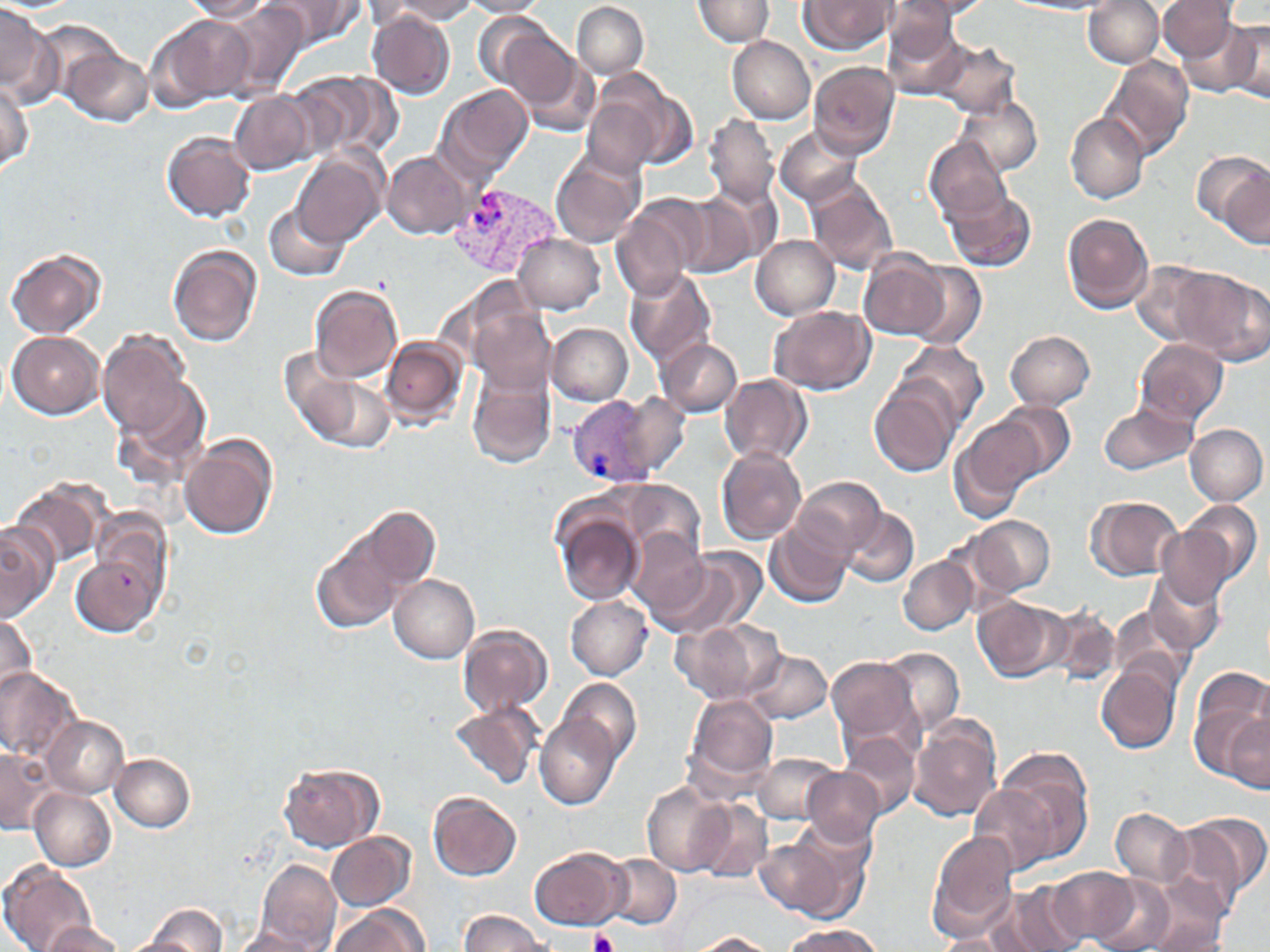

Summary:
  - Coordinate format: approximate bounding boxes as named x1/y1/x2/y2 corners in pixels
  - Uninfected red blood cell locations: (x1=180, y1=0, x2=274, y2=23), (x1=264, y1=0, x2=360, y2=47), (x1=380, y1=0, x2=479, y2=23), (x1=692, y1=0, x2=775, y2=45), (x1=798, y1=0, x2=894, y2=55), (x1=892, y1=0, x2=997, y2=22), (x1=462, y1=1, x2=550, y2=17), (x1=1083, y1=1, x2=1163, y2=67), (x1=1158, y1=1, x2=1242, y2=63), (x1=219, y1=2, x2=312, y2=97), (x1=363, y1=2, x2=455, y2=33), (x1=571, y1=2, x2=648, y2=79), (x1=885, y1=2, x2=984, y2=49), (x1=0, y1=3, x2=56, y2=100), (x1=366, y1=10, x2=456, y2=100), (x1=881, y1=11, x2=974, y2=99), (x1=472, y1=12, x2=557, y2=89), (x1=158, y1=14, x2=253, y2=106), (x1=1169, y1=15, x2=1264, y2=102), (x1=1225, y1=18, x2=1270, y2=103), (x1=495, y1=26, x2=582, y2=111), (x1=727, y1=36, x2=815, y2=123), (x1=932, y1=41, x2=1016, y2=119), (x1=62, y1=45, x2=151, y2=127), (x1=515, y1=49, x2=601, y2=136), (x1=1103, y1=56, x2=1194, y2=160), (x1=809, y1=61, x2=900, y2=159), (x1=593, y1=69, x2=697, y2=172), (x1=286, y1=71, x2=388, y2=162), (x1=0, y1=76, x2=33, y2=172), (x1=437, y1=84, x2=532, y2=181), (x1=229, y1=90, x2=316, y2=176), (x1=954, y1=93, x2=1042, y2=178), (x1=583, y1=96, x2=658, y2=176), (x1=1065, y1=111, x2=1149, y2=202), (x1=705, y1=114, x2=779, y2=210), (x1=776, y1=126, x2=862, y2=208), (x1=162, y1=131, x2=256, y2=221), (x1=924, y1=136, x2=1013, y2=225), (x1=293, y1=150, x2=386, y2=248), (x1=1192, y1=150, x2=1270, y2=237), (x1=552, y1=151, x2=645, y2=248), (x1=383, y1=152, x2=468, y2=239), (x1=806, y1=175, x2=900, y2=276), (x1=709, y1=184, x2=783, y2=266), (x1=944, y1=187, x2=1036, y2=272), (x1=676, y1=190, x2=764, y2=278), (x1=612, y1=195, x2=705, y2=299), (x1=264, y1=199, x2=349, y2=282), (x1=1062, y1=212, x2=1155, y2=314), (x1=514, y1=233, x2=605, y2=313), (x1=752, y1=235, x2=839, y2=320), (x1=168, y1=244, x2=262, y2=346), (x1=7, y1=248, x2=107, y2=339), (x1=858, y1=251, x2=954, y2=343), (x1=1132, y1=259, x2=1217, y2=347), (x1=908, y1=262, x2=986, y2=349), (x1=1171, y1=266, x2=1267, y2=365), (x1=624, y1=269, x2=718, y2=370), (x1=310, y1=285, x2=402, y2=384), (x1=468, y1=303, x2=557, y2=397), (x1=769, y1=305, x2=876, y2=395), (x1=547, y1=324, x2=633, y2=406), (x1=98, y1=329, x2=197, y2=440), (x1=1005, y1=330, x2=1096, y2=411), (x1=7, y1=331, x2=104, y2=419), (x1=382, y1=337, x2=468, y2=429), (x1=1134, y1=337, x2=1229, y2=426), (x1=657, y1=338, x2=743, y2=416), (x1=896, y1=341, x2=988, y2=432), (x1=282, y1=346, x2=393, y2=450), (x1=467, y1=367, x2=557, y2=471), (x1=719, y1=374, x2=813, y2=464), (x1=115, y1=376, x2=212, y2=483), (x1=870, y1=381, x2=960, y2=478), (x1=617, y1=392, x2=687, y2=478), (x1=995, y1=401, x2=1076, y2=481), (x1=1098, y1=403, x2=1197, y2=477), (x1=951, y1=416, x2=1045, y2=516), (x1=1186, y1=424, x2=1267, y2=506), (x1=178, y1=435, x2=278, y2=540), (x1=716, y1=446, x2=806, y2=543), (x1=792, y1=475, x2=888, y2=561), (x1=615, y1=478, x2=707, y2=571), (x1=12, y1=479, x2=107, y2=570), (x1=1086, y1=495, x2=1183, y2=580), (x1=1184, y1=501, x2=1262, y2=586), (x1=840, y1=504, x2=920, y2=589), (x1=364, y1=506, x2=438, y2=589), (x1=554, y1=507, x2=645, y2=604), (x1=965, y1=514, x2=1057, y2=594), (x1=765, y1=518, x2=854, y2=609), (x1=0, y1=521, x2=56, y2=624), (x1=1157, y1=525, x2=1237, y2=606), (x1=627, y1=529, x2=714, y2=620), (x1=312, y1=537, x2=402, y2=633), (x1=650, y1=548, x2=764, y2=641), (x1=72, y1=554, x2=160, y2=636), (x1=899, y1=555, x2=977, y2=635), (x1=1144, y1=568, x2=1225, y2=657), (x1=389, y1=574, x2=479, y2=663), (x1=566, y1=595, x2=652, y2=680), (x1=973, y1=596, x2=1065, y2=682), (x1=1042, y1=602, x2=1123, y2=686), (x1=1109, y1=606, x2=1190, y2=686), (x1=0, y1=611, x2=39, y2=703), (x1=673, y1=617, x2=786, y2=704), (x1=458, y1=623, x2=553, y2=717), (x1=880, y1=647, x2=965, y2=734), (x1=746, y1=649, x2=832, y2=723), (x1=827, y1=656, x2=922, y2=749), (x1=1097, y1=663, x2=1180, y2=754), (x1=1189, y1=665, x2=1269, y2=776), (x1=0, y1=667, x2=82, y2=762), (x1=559, y1=677, x2=642, y2=763), (x1=685, y1=694, x2=779, y2=788), (x1=449, y1=701, x2=542, y2=790), (x1=535, y1=712, x2=619, y2=809), (x1=1224, y1=713, x2=1270, y2=790), (x1=43, y1=716, x2=128, y2=797), (x1=907, y1=717, x2=1003, y2=821), (x1=839, y1=733, x2=921, y2=820), (x1=0, y1=746, x2=54, y2=834), (x1=752, y1=752, x2=839, y2=823), (x1=995, y1=752, x2=1096, y2=860), (x1=110, y1=753, x2=195, y2=831), (x1=277, y1=760, x2=382, y2=853), (x1=804, y1=768, x2=884, y2=846), (x1=642, y1=781, x2=731, y2=876), (x1=969, y1=785, x2=1058, y2=873), (x1=30, y1=788, x2=115, y2=871), (x1=428, y1=790, x2=522, y2=881), (x1=693, y1=800, x2=773, y2=883), (x1=1110, y1=808, x2=1190, y2=885), (x1=1170, y1=814, x2=1268, y2=913), (x1=326, y1=830, x2=415, y2=909), (x1=928, y1=830, x2=1018, y2=937), (x1=754, y1=832, x2=860, y2=921), (x1=530, y1=846, x2=629, y2=931), (x1=605, y1=854, x2=682, y2=929), (x1=255, y1=860, x2=342, y2=950), (x1=1, y1=863, x2=96, y2=952), (x1=1048, y1=866, x2=1143, y2=945), (x1=1090, y1=875, x2=1177, y2=952), (x1=998, y1=883, x2=1087, y2=952), (x1=1139, y1=901, x2=1232, y2=951), (x1=134, y1=903, x2=229, y2=951), (x1=326, y1=905, x2=427, y2=952), (x1=458, y1=910, x2=557, y2=951), (x1=42, y1=921, x2=124, y2=952), (x1=782, y1=924, x2=883, y2=952), (x1=227, y1=927, x2=327, y2=951), (x1=115, y1=931, x2=214, y2=952), (x1=687, y1=931, x2=781, y2=951), (x1=931, y1=932, x2=1013, y2=951)
  - Plasmodium vivax-infected red blood cell locations: (x1=450, y1=186, x2=559, y2=281), (x1=570, y1=394, x2=658, y2=487)
  - Platelet locations: (x1=117, y1=571, x2=133, y2=588), (x1=590, y1=930, x2=619, y2=952)
  - Slide-level diagnosis: Plasmodium vivax
  - Image size: 1270×952 pixels
  - Field of view: one of a larger specimen
  - Modality: optical microscopy
  - Preparation: thin blood film
  - Stain: May-Grünwald-Giemsa
  - Magnification: 1000x